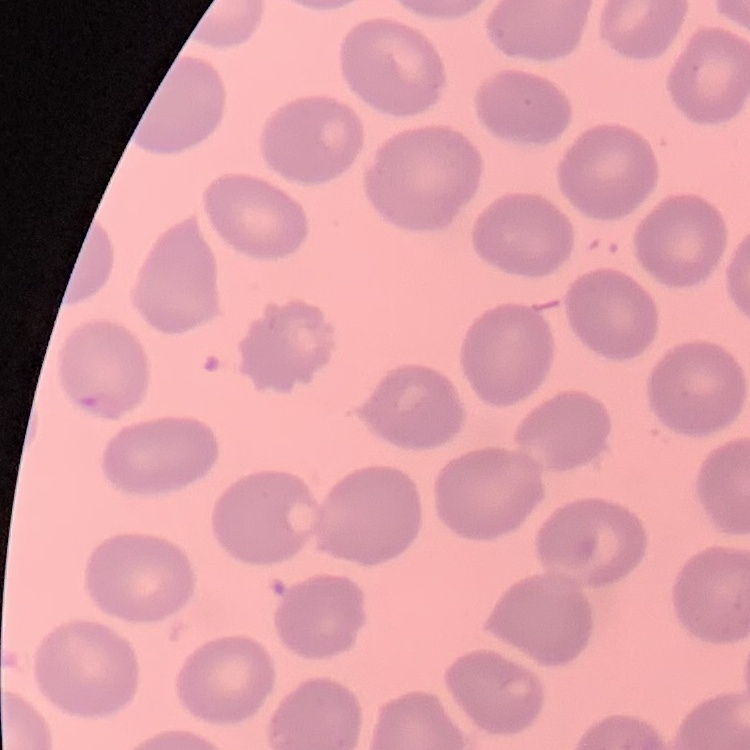
red blood cell morphology = no rouleaux formation
image type = square crop of a larger photomicrograph
stain = Field's or Giemsa
preparation = thin blood smear